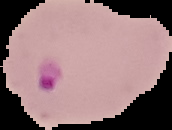

Summary:
  - Malaria status: parasitized
  - Image type: segmented cell region on a black background
  - Preparation: thin blood film
  - Image size: 172×130 pixels